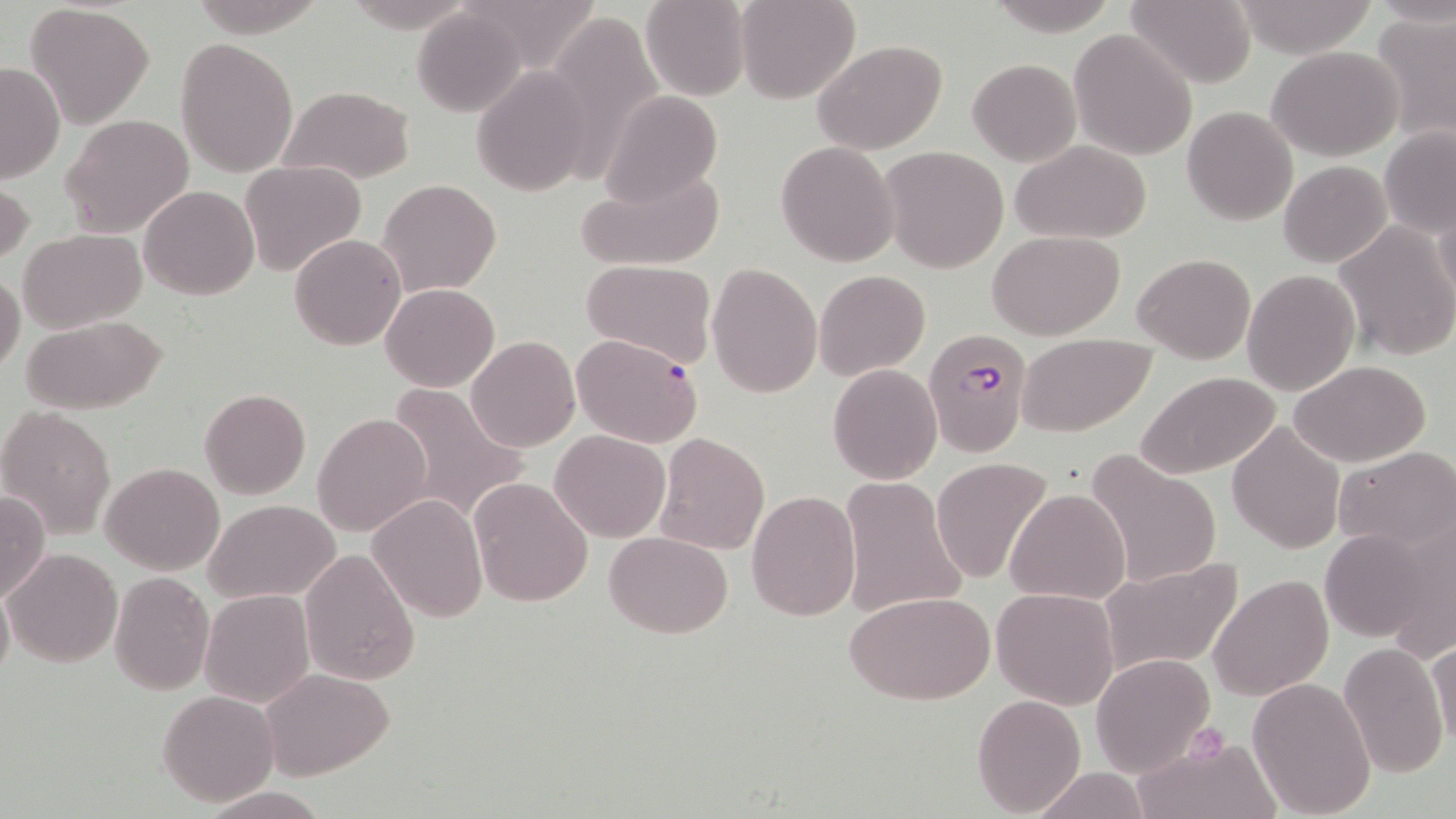

slide-level diagnosis = Plasmodium falciparum
stain = May-Grünwald-Giemsa
preparation = thin blood smear
uninfected red blood cell locations = approximate bounding boxes as [x1, y1, x2, y2] in pixels: [460, 0, 602, 71], [641, 0, 752, 102], [735, 0, 859, 104], [1127, 0, 1255, 88], [1229, 1, 1380, 57], [24, 4, 154, 128], [411, 7, 526, 117], [541, 11, 664, 171], [1372, 12, 1456, 147], [1068, 28, 1198, 161], [176, 37, 298, 178], [813, 39, 948, 153], [1267, 46, 1404, 160], [967, 58, 1080, 166], [0, 63, 65, 183], [470, 67, 595, 197], [279, 85, 415, 185], [599, 90, 724, 207], [1182, 105, 1298, 226], [61, 114, 194, 237], [1378, 126, 1454, 237], [776, 140, 900, 267], [1010, 140, 1154, 243], [878, 146, 1010, 273], [240, 160, 368, 277], [574, 161, 727, 272], [1279, 161, 1391, 267], [1, 177, 34, 268], [378, 178, 501, 297], [138, 185, 259, 300], [1431, 195, 1456, 306], [1334, 219, 1455, 361], [18, 228, 147, 332], [985, 229, 1125, 340], [288, 234, 407, 351], [1133, 252, 1256, 364], [580, 259, 718, 368], [706, 260, 823, 399], [813, 268, 930, 381], [1242, 269, 1360, 395], [0, 271, 25, 373], [381, 283, 500, 391], [20, 315, 167, 413], [1015, 333, 1157, 438], [465, 336, 579, 452], [1290, 359, 1433, 466], [827, 364, 942, 483], [1133, 369, 1283, 480], [385, 381, 528, 524], [199, 389, 311, 499], [1, 408, 116, 538], [312, 413, 432, 536], [1227, 422, 1345, 553], [550, 430, 671, 543], [653, 431, 771, 556], [1334, 446, 1456, 553], [1085, 448, 1223, 589], [931, 457, 1055, 586], [100, 462, 223, 574], [839, 476, 969, 620], [470, 477, 594, 608], [746, 488, 861, 622], [1005, 489, 1128, 604], [0, 490, 49, 605], [367, 494, 488, 621], [204, 499, 340, 603], [1384, 514, 1456, 661], [1319, 527, 1439, 642], [604, 532, 731, 638], [4, 547, 122, 666], [299, 548, 420, 686], [1098, 554, 1246, 677], [108, 572, 214, 694], [1209, 572, 1332, 701], [0, 579, 13, 690], [992, 588, 1120, 710], [199, 589, 315, 708], [844, 590, 996, 707], [1428, 639, 1455, 752], [1337, 643, 1449, 777], [1090, 653, 1216, 776], [258, 668, 397, 781], [1247, 676, 1376, 815], [157, 691, 280, 808], [971, 693, 1086, 814], [1131, 734, 1281, 819], [1030, 767, 1153, 819], [198, 786, 331, 818]
field of view = single
image size = 1456×819 pixels
magnification = 1000x
modality = light microscopy
Plasmodium falciparum-infected red blood cell locations = approximate bounding boxes as [x1, y1, x2, y2] in pixels: [923, 328, 1031, 457], [572, 334, 704, 448]